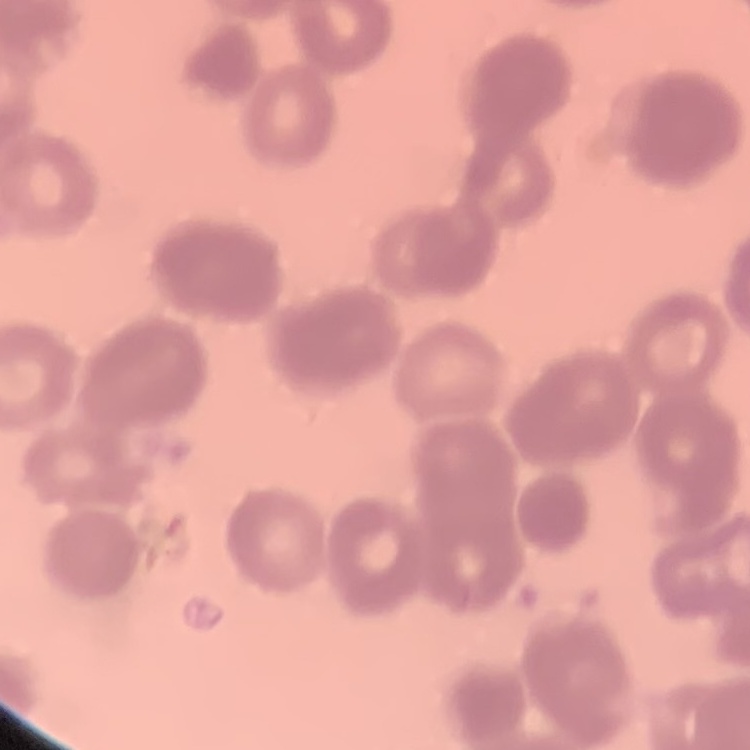
erythrocyte morphology = rouleaux formation
image type = one tile cut from a larger photomicrograph
stain = Field's or Giemsa
preparation = thin blood film